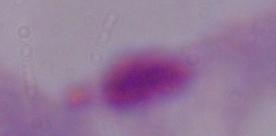
A trichomonad is seen. Captured at 1000x magnification. Micrograph.